Give the extent of all Trypanosoma brucei.
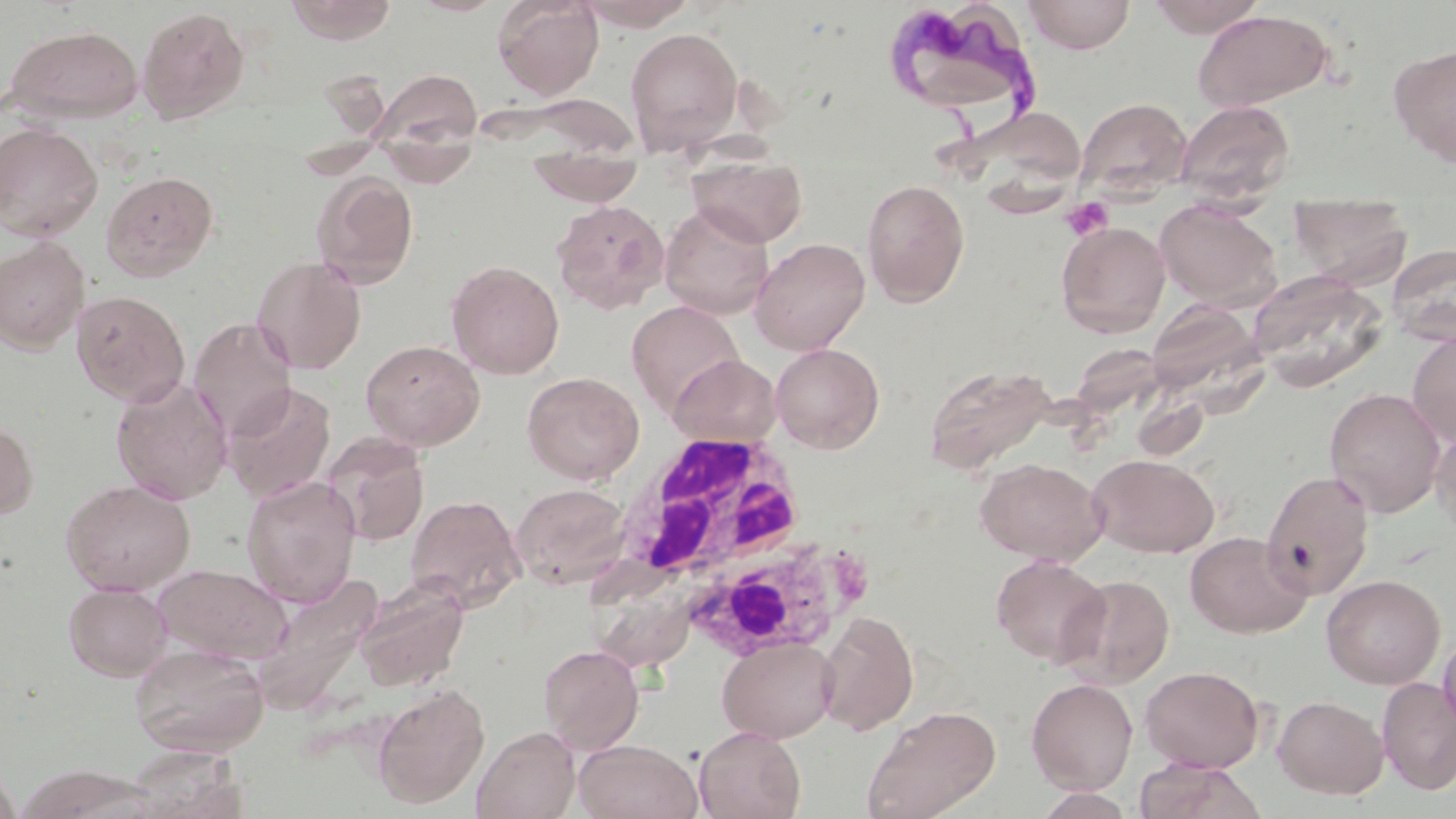

Approximate bounding boxes as (x1, y1, x2, y2) in pixels.
Trypanosoma brucei: (878, 2, 1046, 127).

slide_level_diagnosis: Trypanosoma brucei
field_of_view: one of a larger specimen
uninfected_red_blood_cell_locations: 'approximate bounding boxes as (x1, y1, x2, y2) in pixels: (285, 0, 397, 44), (492, 0, 604, 99), (1023, 0, 1136, 54), (1145, 0, 1267, 37), (575, 1, 699, 29), (137, 6, 250, 124), (1192, 9, 1335, 112), (4, 24, 144, 123), (625, 26, 744, 156), (1390, 44, 1456, 166), (369, 69, 482, 162), (1074, 97, 1192, 200), (1175, 100, 1295, 204), (951, 105, 1088, 203), (0, 122, 103, 242), (527, 148, 645, 207), (688, 152, 808, 247), (100, 170, 219, 282), (311, 171, 420, 289), (861, 178, 970, 306), (1288, 192, 1412, 287), (552, 199, 670, 314), (1155, 199, 1281, 309), (659, 202, 774, 319), (1056, 220, 1171, 337), (750, 237, 870, 355), (0, 238, 90, 353), (1386, 243, 1456, 345), (252, 255, 367, 374), (446, 260, 564, 378), (1249, 273, 1388, 390), (71, 290, 190, 407), (626, 300, 746, 419), (1145, 301, 1262, 398), (188, 318, 297, 440), (1407, 330, 1456, 446), (360, 339, 484, 451), (771, 343, 884, 453), (668, 354, 782, 447), (924, 362, 1059, 473), (522, 371, 644, 484), (111, 376, 233, 504), (223, 383, 336, 502), (1324, 387, 1446, 517), (0, 419, 38, 521), (1430, 420, 1456, 539), (321, 433, 429, 547), (1088, 453, 1219, 557), (975, 457, 1108, 564), (1261, 469, 1375, 600), (241, 476, 361, 607), (60, 479, 195, 595), (511, 483, 631, 589), (406, 494, 526, 612), (1184, 531, 1310, 638), (990, 554, 1110, 666), (591, 557, 692, 663), (152, 563, 292, 664), (254, 572, 383, 710), (1060, 574, 1175, 688), (1321, 574, 1445, 689), (353, 578, 469, 692), (63, 581, 172, 681), (816, 610, 919, 735), (1437, 629, 1456, 739), (718, 636, 838, 743), (129, 643, 270, 757), (538, 643, 644, 753), (1140, 665, 1264, 772), (1377, 676, 1456, 794), (1026, 678, 1138, 794), (372, 684, 489, 809), (1273, 695, 1388, 799), (860, 704, 1001, 819), (472, 725, 581, 819), (693, 725, 806, 819), (573, 739, 703, 819), (123, 747, 250, 818), (1132, 758, 1263, 819), (0, 761, 21, 819), (15, 764, 154, 818), (1032, 788, 1137, 819)'
platelet_locations: 'approximate bounding boxes as (x1, y1, x2, y2) in pixels: (1059, 197, 1112, 240)'
magnification: 1000x
preparation: thin blood film
white_blood_cell_locations: 'approximate bounding boxes as (x1, y1, x2, y2) in pixels: (609, 432, 869, 637)'
image_size: 1456×819 pixels
stain: May-Grünwald-Giemsa
modality: light microscopy